Locate every uninfected red blood cell.
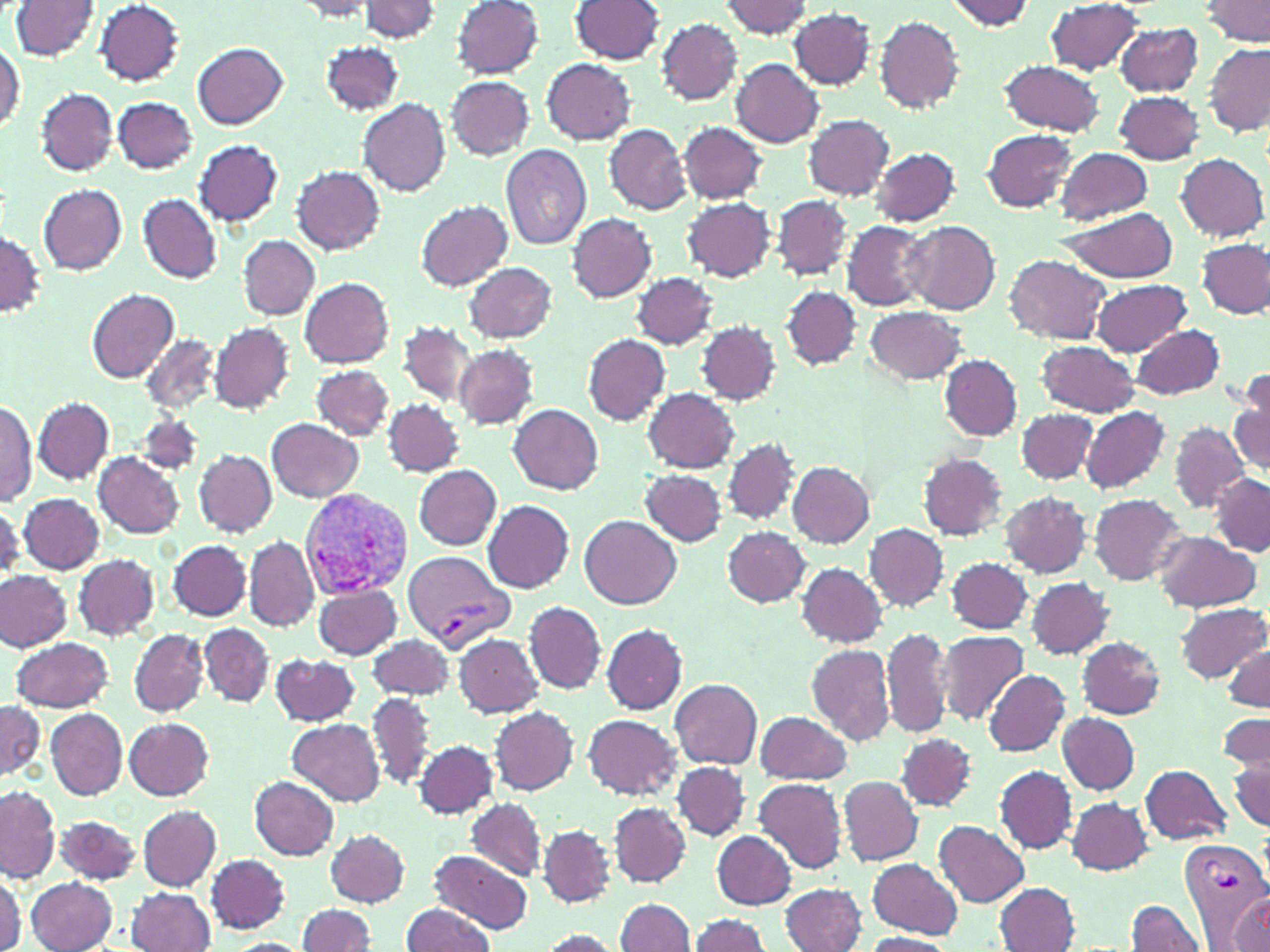
Approximate bounding boxes as (x1,y1)-(x2,y2) corner pairs in pixels.
Uninfected red blood cells: (452,0)-(545,78), (570,0)-(665,64), (944,0)-(1038,31), (1202,0)-(1270,47), (12,1)-(99,58), (95,1)-(185,84), (291,1)-(382,20), (356,1)-(443,42), (720,2)-(816,39), (1044,2)-(1147,76), (789,8)-(876,88), (874,16)-(965,113), (657,18)-(743,105), (1115,23)-(1203,95), (0,40)-(24,134), (320,42)-(404,116), (193,43)-(288,129), (1204,43)-(1269,134), (541,58)-(636,144), (731,58)-(825,147), (997,60)-(1107,136), (445,75)-(535,159), (35,88)-(117,176), (1114,91)-(1204,164), (113,96)-(198,174), (359,99)-(451,196), (803,114)-(894,200), (678,122)-(767,205), (604,124)-(690,214), (981,129)-(1078,212), (193,140)-(283,226), (500,145)-(591,250), (1055,146)-(1153,225), (868,147)-(962,227), (1175,152)-(1268,241), (292,166)-(385,255), (40,185)-(128,274), (138,194)-(222,284), (773,196)-(853,280), (683,197)-(776,282), (416,201)-(513,290), (1057,206)-(1179,283), (567,214)-(657,303), (842,220)-(930,310), (902,220)-(1001,314), (0,231)-(45,319), (238,235)-(320,319), (1197,238)-(1270,318), (1004,254)-(1112,345), (463,261)-(558,343), (631,272)-(720,349), (300,277)-(395,368), (1090,279)-(1193,356), (782,286)-(862,369), (87,288)-(179,384), (866,305)-(966,384), (696,321)-(781,405), (210,322)-(294,413), (400,322)-(477,406), (1131,323)-(1226,400), (141,333)-(218,412), (583,334)-(671,425), (1035,340)-(1140,419), (454,345)-(539,429), (938,355)-(1022,441), (311,365)-(394,440), (1229,378)-(1270,477), (644,387)-(738,473), (34,397)-(113,483), (0,398)-(37,507), (384,399)-(466,476), (509,404)-(604,494), (1081,406)-(1170,492), (1017,408)-(1098,485), (267,417)-(365,503), (1168,422)-(1250,513), (723,437)-(802,524), (195,449)-(276,536), (917,451)-(1008,541), (92,452)-(184,538), (787,461)-(874,548), (413,465)-(502,550), (641,469)-(726,547), (1210,472)-(1270,555), (1000,490)-(1091,578), (18,493)-(104,574), (1089,494)-(1186,584), (483,500)-(575,593), (0,502)-(23,578), (580,515)-(681,609), (864,523)-(948,610), (722,526)-(812,608), (1152,533)-(1261,613), (243,536)-(317,631), (168,539)-(250,621), (72,553)-(160,639), (945,556)-(1035,635), (796,563)-(888,647), (1,569)-(71,652), (1025,578)-(1114,658), (311,582)-(403,659), (524,600)-(607,694), (1173,602)-(1269,683), (199,624)-(275,708), (601,624)-(687,715), (883,626)-(953,740), (129,628)-(209,717), (936,628)-(1029,726), (454,632)-(543,717), (368,635)-(454,700), (1076,636)-(1167,719), (12,637)-(115,711), (1223,642)-(1269,712), (805,644)-(895,745), (271,654)-(359,726), (983,669)-(1070,755), (669,679)-(763,768), (366,692)-(437,790), (0,698)-(43,784), (45,707)-(128,799), (489,707)-(577,795), (756,709)-(853,785), (1059,712)-(1140,793), (583,713)-(681,799), (1062,714)-(1145,873), (1218,714)-(1269,783), (124,717)-(215,800), (286,719)-(385,805), (895,732)-(977,811), (414,740)-(497,818), (1230,749)-(1270,831), (672,761)-(751,840), (1139,764)-(1231,844), (995,766)-(1076,853), (838,775)-(923,866), (248,776)-(340,861), (754,778)-(847,875), (0,787)-(58,882), (1066,798)-(1153,873), (467,800)-(547,878), (610,802)-(690,886), (137,805)-(221,891), (55,815)-(141,885), (934,820)-(1031,907), (536,824)-(616,907), (326,830)-(409,907), (712,831)-(796,909), (429,851)-(534,932), (205,854)-(291,934), (867,858)-(963,938), (128,870)-(291,944), (0,871)-(23,950), (26,877)-(118,952), (995,882)-(1079,951), (781,883)-(867,952), (124,888)-(217,952), (1227,891)-(1270,948), (616,897)-(694,952), (1125,898)-(1207,951), (297,903)-(376,951), (400,904)-(496,952), (688,913)-(771,952), (534,929)-(621,952), (860,932)-(959,952).

Plasmodium vivax-infected red blood cell locations = approximate bounding boxes as (x1,y1)-(x2,y2) corner pairs in pixels: (299,490)-(414,597), (404,550)-(512,651), (1177,837)-(1269,937)
slide-level diagnosis = Plasmodium vivax
magnification = 1000x
modality = optical microscopy
field of view = single
preparation = thin blood film
image size = 1270×952 pixels
stain = May-Grünwald-Giemsa